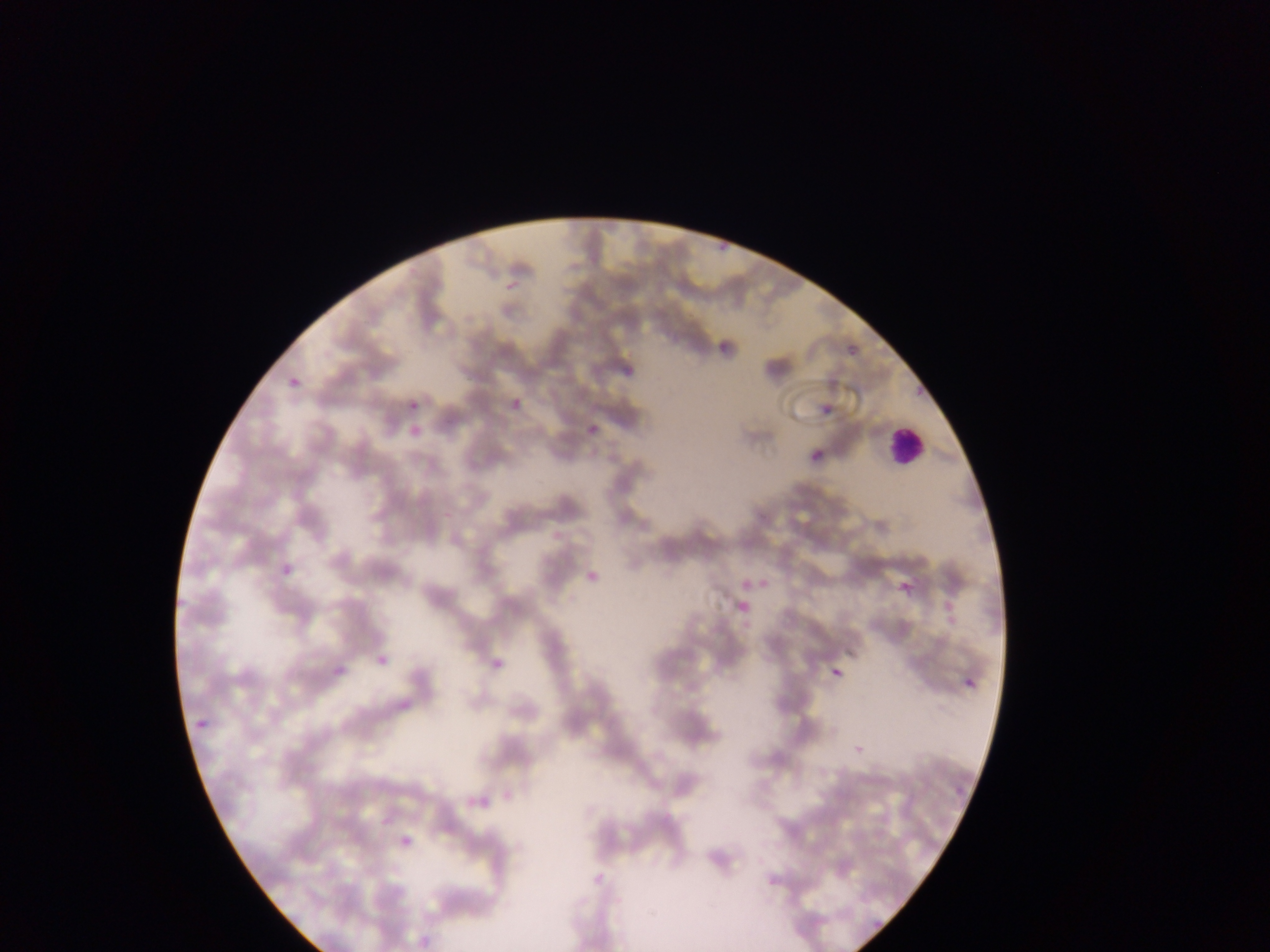

capture: mobile-phone photograph through a microscope
preparation: thin blood smear
image_size: 1270×952 pixels
country: Ghana
field_of_view: single
plasmodium_parasite_locations: 'approximate bounding boxes as [left, top, right, bottom] in pixels: [713, 234, 730, 255], [500, 276, 527, 297], [708, 338, 735, 360], [848, 345, 858, 355], [613, 365, 639, 385], [286, 369, 304, 386], [506, 395, 524, 418], [408, 400, 419, 411], [820, 403, 834, 415], [578, 420, 608, 438], [405, 423, 425, 445], [810, 450, 822, 462], [274, 535, 297, 576], [580, 570, 601, 593], [758, 572, 779, 591], [736, 574, 755, 591], [891, 577, 922, 600], [732, 597, 754, 615], [482, 649, 516, 676], [372, 650, 392, 670], [826, 658, 850, 678], [328, 666, 347, 686], [961, 669, 985, 696], [392, 702, 411, 717], [191, 711, 210, 739], [854, 734, 873, 751], [499, 778, 525, 806], [949, 780, 970, 804], [465, 791, 488, 814], [399, 838, 413, 851], [587, 858, 620, 889], [769, 875, 783, 886], [864, 915, 891, 938], [412, 927, 430, 952]'
leukocyte_locations: 'approximate bounding boxes as [left, top, right, bottom] in pixels: [889, 423, 928, 467]'